Draw a bounding box around every parasitised red blood cell.
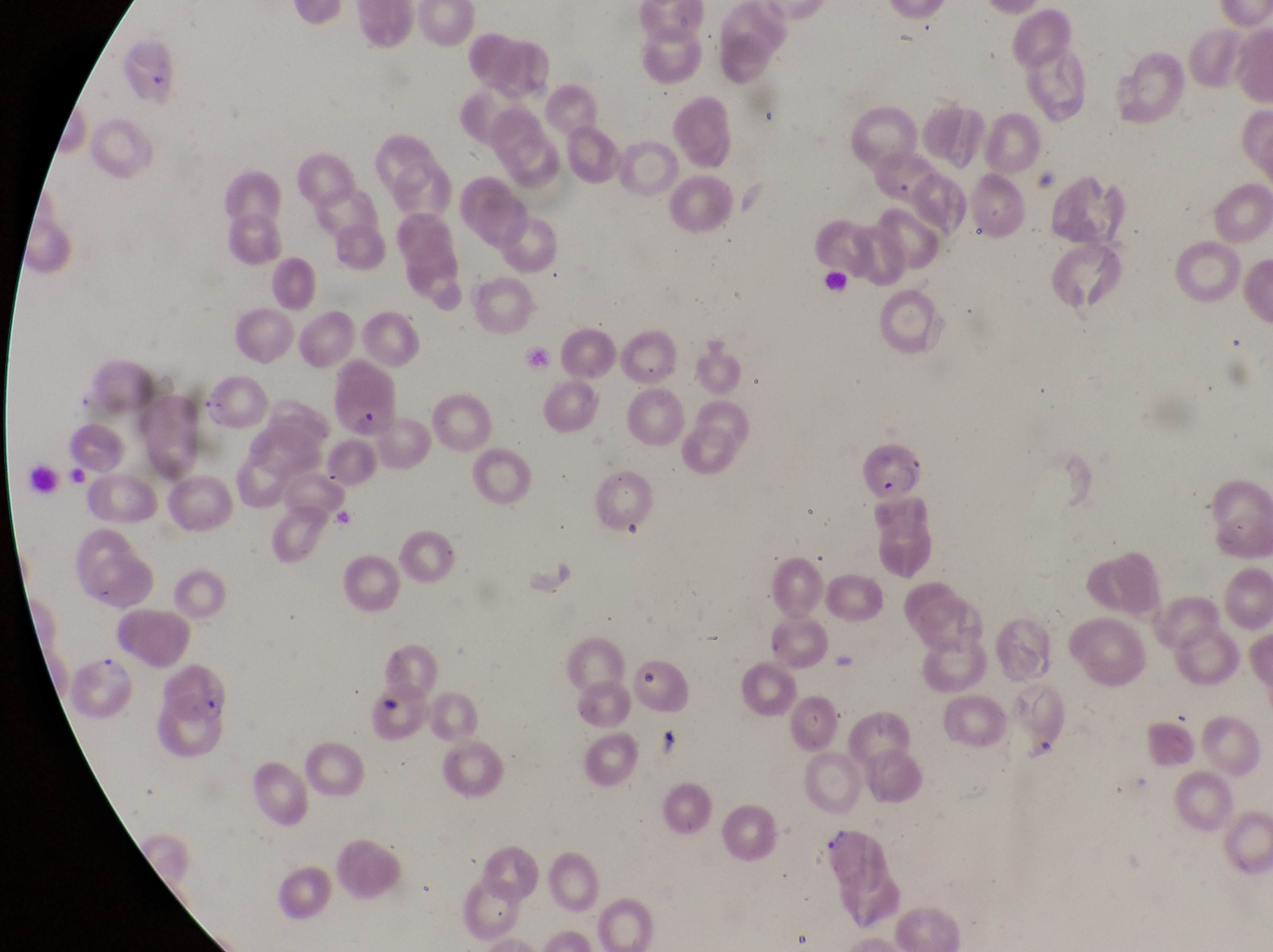
Approximate bounding boxes as (left, top, right, bottom) in pixels.
Parasitised red blood cells: (204, 375, 274, 432), (861, 445, 931, 507), (70, 656, 140, 721), (160, 668, 230, 730).

{
  "capture": "smartphone photograph through the eyepiece of an Olympus CX-23 microscope",
  "preparation": "thin blood smear",
  "image_size": "1273×952 pixels",
  "country": "Uganda",
  "field_of_view": "single",
  "magnification": "1000x",
  "artifact_platelet_like_body_stain_precipitate_or_debris_locations": "approximate bounding boxes as (left, top, right, bottom) in pixels: (352, 407, 382, 437)"
}